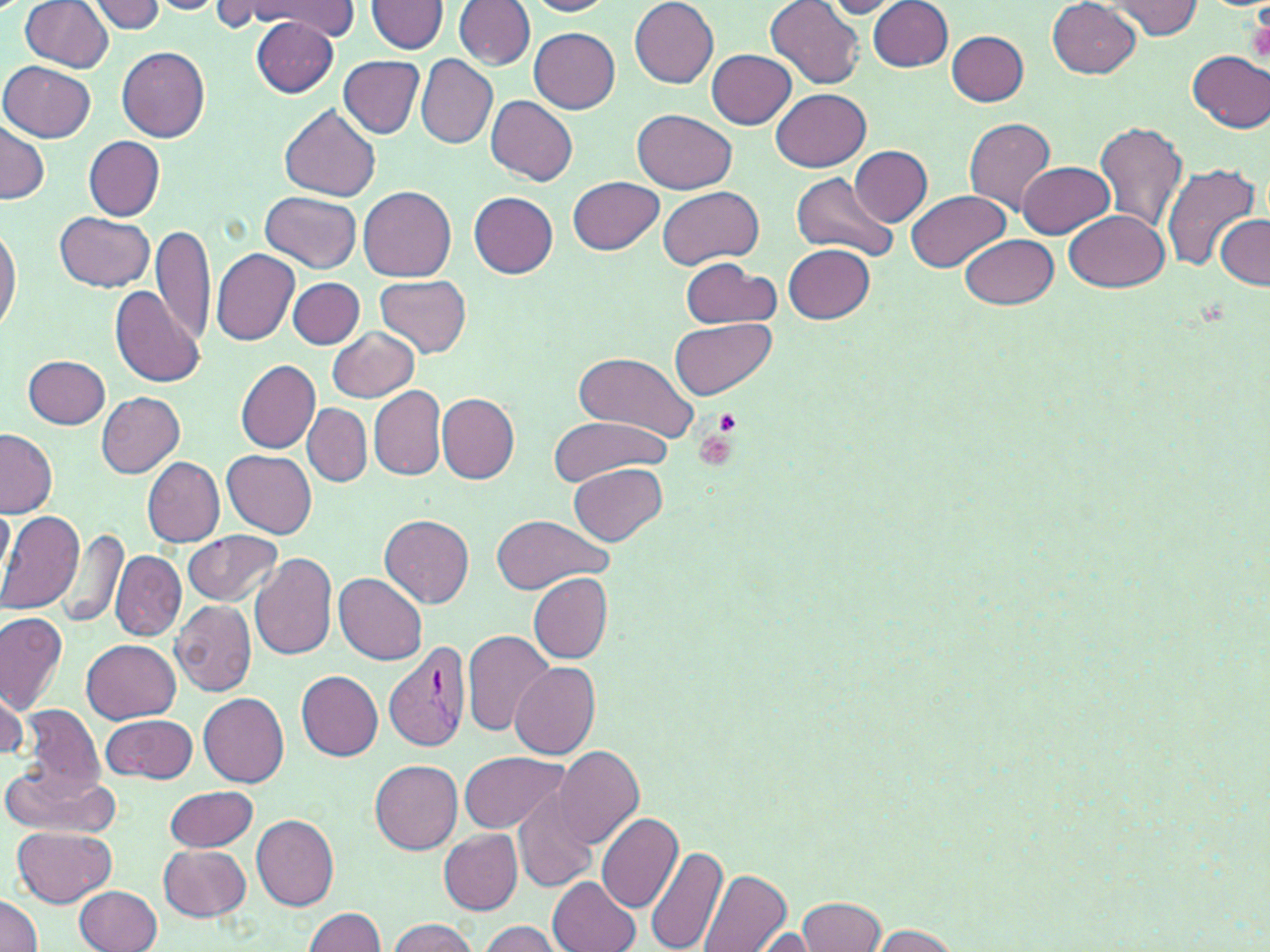 Approximate bounding boxes as named x1/y1/x2/y2 corners in pixels. Uninfected red blood cell locations: (x1=244, y1=0, x2=358, y2=37), (x1=522, y1=0, x2=615, y2=17), (x1=628, y1=0, x2=718, y2=88), (x1=19, y1=1, x2=115, y2=72), (x1=91, y1=1, x2=167, y2=34), (x1=147, y1=1, x2=222, y2=15), (x1=368, y1=1, x2=447, y2=53), (x1=455, y1=1, x2=535, y2=69), (x1=766, y1=1, x2=865, y2=87), (x1=819, y1=1, x2=909, y2=17), (x1=869, y1=1, x2=952, y2=72), (x1=1048, y1=1, x2=1143, y2=78), (x1=1099, y1=1, x2=1203, y2=39), (x1=208, y1=3, x2=294, y2=28), (x1=250, y1=17, x2=338, y2=99), (x1=530, y1=29, x2=621, y2=113), (x1=947, y1=30, x2=1029, y2=106), (x1=116, y1=45, x2=210, y2=140), (x1=707, y1=49, x2=797, y2=129), (x1=1187, y1=50, x2=1270, y2=132), (x1=415, y1=54, x2=498, y2=149), (x1=339, y1=57, x2=425, y2=138), (x1=2, y1=61, x2=98, y2=142), (x1=772, y1=88, x2=871, y2=171), (x1=485, y1=94, x2=577, y2=185), (x1=279, y1=105, x2=381, y2=202), (x1=635, y1=110, x2=735, y2=194), (x1=963, y1=117, x2=1057, y2=216), (x1=0, y1=119, x2=49, y2=206), (x1=1094, y1=120, x2=1190, y2=235), (x1=84, y1=135, x2=165, y2=221), (x1=852, y1=146, x2=933, y2=225), (x1=1019, y1=161, x2=1115, y2=238), (x1=1162, y1=163, x2=1260, y2=276), (x1=791, y1=174, x2=897, y2=260), (x1=568, y1=176, x2=664, y2=254), (x1=359, y1=186, x2=455, y2=279), (x1=656, y1=186, x2=764, y2=269), (x1=468, y1=190, x2=558, y2=278), (x1=906, y1=190, x2=1010, y2=273), (x1=260, y1=191, x2=361, y2=271), (x1=1064, y1=209, x2=1171, y2=291), (x1=55, y1=210, x2=155, y2=291), (x1=1214, y1=215, x2=1269, y2=288), (x1=0, y1=217, x2=20, y2=340), (x1=152, y1=223, x2=216, y2=345), (x1=960, y1=235, x2=1058, y2=308), (x1=784, y1=243, x2=876, y2=322), (x1=210, y1=249, x2=302, y2=345), (x1=679, y1=259, x2=779, y2=330), (x1=374, y1=274, x2=472, y2=358), (x1=288, y1=278, x2=365, y2=348), (x1=109, y1=289, x2=206, y2=389), (x1=672, y1=317, x2=776, y2=400), (x1=327, y1=325, x2=418, y2=403), (x1=573, y1=351, x2=701, y2=443), (x1=23, y1=354, x2=111, y2=429), (x1=237, y1=360, x2=320, y2=453), (x1=368, y1=384, x2=447, y2=481), (x1=95, y1=391, x2=186, y2=477), (x1=436, y1=393, x2=520, y2=483), (x1=301, y1=405, x2=371, y2=487), (x1=547, y1=416, x2=670, y2=488), (x1=0, y1=428, x2=56, y2=517), (x1=222, y1=450, x2=317, y2=538), (x1=143, y1=458, x2=225, y2=546), (x1=569, y1=462, x2=666, y2=546), (x1=0, y1=501, x2=14, y2=581), (x1=0, y1=511, x2=86, y2=615), (x1=378, y1=513, x2=474, y2=608), (x1=489, y1=514, x2=610, y2=594), (x1=55, y1=528, x2=130, y2=630), (x1=183, y1=531, x2=283, y2=607), (x1=112, y1=550, x2=185, y2=640), (x1=249, y1=554, x2=338, y2=662), (x1=334, y1=573, x2=428, y2=665), (x1=530, y1=573, x2=613, y2=663), (x1=169, y1=598, x2=257, y2=697), (x1=0, y1=613, x2=68, y2=713), (x1=462, y1=628, x2=556, y2=736), (x1=82, y1=638, x2=182, y2=722), (x1=509, y1=661, x2=601, y2=758), (x1=295, y1=669, x2=384, y2=761), (x1=0, y1=679, x2=27, y2=762), (x1=199, y1=693, x2=289, y2=786), (x1=18, y1=703, x2=104, y2=799), (x1=102, y1=714, x2=198, y2=785), (x1=553, y1=746, x2=644, y2=848), (x1=459, y1=752, x2=568, y2=833), (x1=370, y1=759, x2=464, y2=852), (x1=2, y1=762, x2=119, y2=837), (x1=543, y1=763, x2=661, y2=900), (x1=164, y1=784, x2=258, y2=853), (x1=512, y1=785, x2=598, y2=892), (x1=596, y1=813, x2=684, y2=914), (x1=251, y1=814, x2=339, y2=911), (x1=11, y1=827, x2=117, y2=907), (x1=438, y1=828, x2=523, y2=913), (x1=159, y1=844, x2=251, y2=921), (x1=645, y1=844, x2=728, y2=952), (x1=698, y1=868, x2=791, y2=952), (x1=549, y1=875, x2=642, y2=952), (x1=75, y1=884, x2=163, y2=952), (x1=0, y1=894, x2=44, y2=951), (x1=796, y1=897, x2=886, y2=952), (x1=303, y1=908, x2=387, y2=951), (x1=384, y1=917, x2=479, y2=952), (x1=475, y1=920, x2=565, y2=952), (x1=865, y1=925, x2=963, y2=951), (x1=740, y1=927, x2=824, y2=950). Platelet locations: (x1=1244, y1=13, x2=1270, y2=69), (x1=712, y1=409, x2=742, y2=436), (x1=693, y1=430, x2=737, y2=472). Plasmodium vivax-infected red blood cell locations: (x1=382, y1=641, x2=472, y2=753). Slide-level diagnosis: Plasmodium vivax. Optical microscopy. 1000x magnification. Image is 1270×952 pixels. Thin blood smear. One field of a larger specimen. May-Grünwald-Giemsa-stained preparation.